Assess the morphology of the red blood cells.
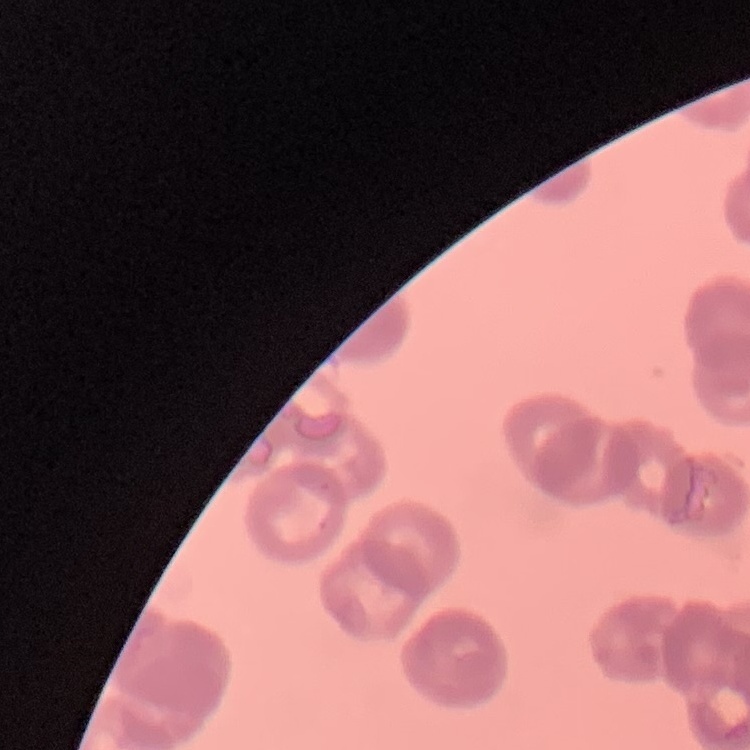
They show rouleaux formation.

stain = Field's or Giemsa
image type = one tile cut from a larger photomicrograph
preparation = thin peripheral smear